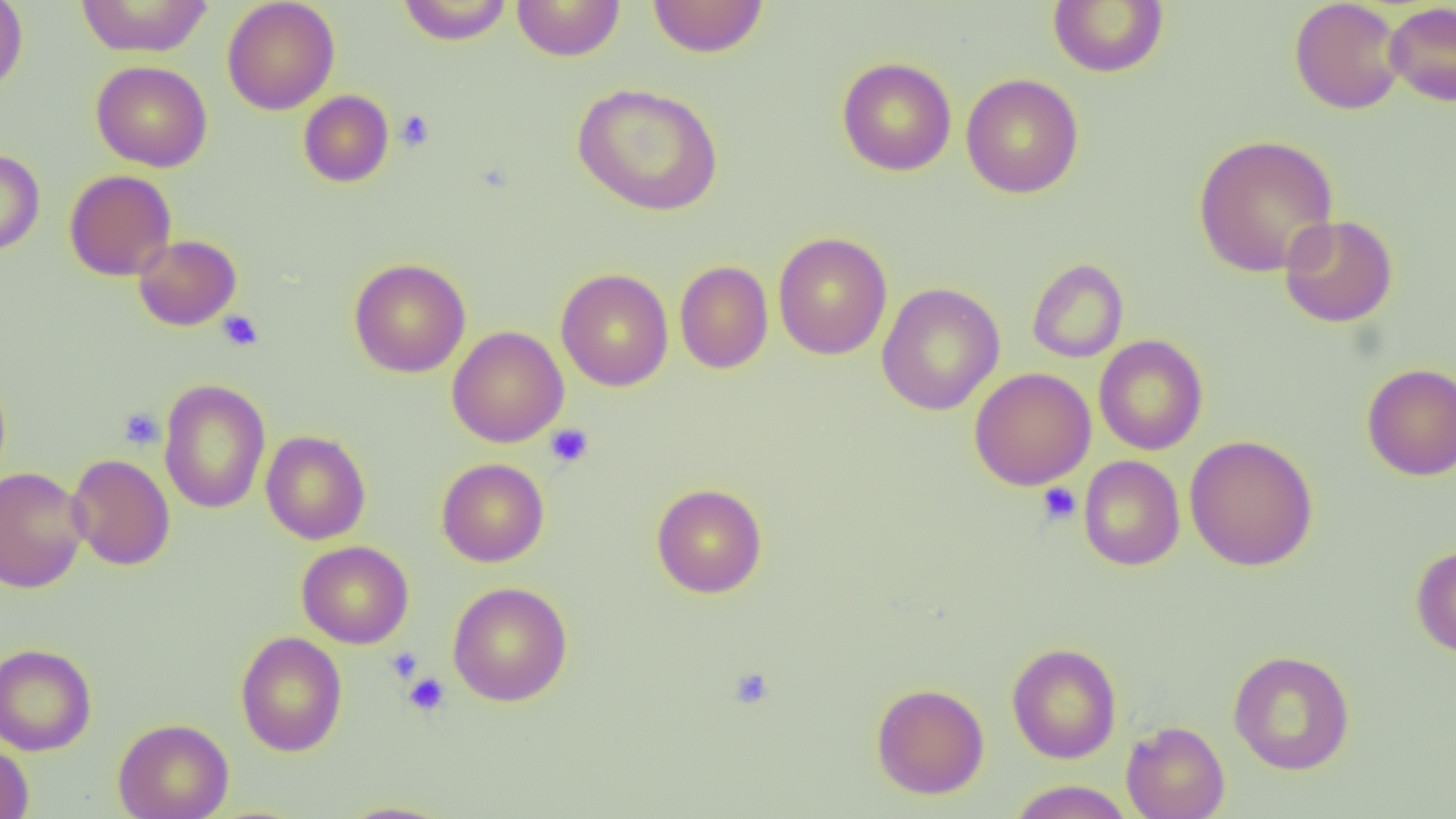
Summary:
  - Coordinate format: approximate bounding boxes as named x1/y1/x2/y2 corners in pixels
  - Platelet locations: (x1=395, y1=110, x2=435, y2=151), (x1=217, y1=310, x2=264, y2=352), (x1=118, y1=408, x2=164, y2=450), (x1=545, y1=423, x2=594, y2=468), (x1=1037, y1=483, x2=1081, y2=526), (x1=386, y1=646, x2=423, y2=683), (x1=728, y1=666, x2=775, y2=710), (x1=403, y1=672, x2=450, y2=716)
  - Uninfected red blood cell locations: (x1=0, y1=0, x2=28, y2=94), (x1=76, y1=0, x2=213, y2=58), (x1=222, y1=0, x2=340, y2=115), (x1=512, y1=0, x2=625, y2=61), (x1=647, y1=0, x2=769, y2=57), (x1=1289, y1=0, x2=1407, y2=115), (x1=397, y1=1, x2=512, y2=45), (x1=1048, y1=1, x2=1169, y2=77), (x1=1384, y1=1, x2=1456, y2=107), (x1=837, y1=57, x2=957, y2=176), (x1=91, y1=60, x2=212, y2=172), (x1=961, y1=73, x2=1084, y2=198), (x1=572, y1=82, x2=723, y2=216), (x1=298, y1=90, x2=394, y2=187), (x1=1193, y1=134, x2=1339, y2=277), (x1=0, y1=148, x2=44, y2=256), (x1=64, y1=169, x2=177, y2=281), (x1=1278, y1=214, x2=1398, y2=328), (x1=773, y1=232, x2=893, y2=360), (x1=132, y1=234, x2=242, y2=331), (x1=673, y1=257, x2=885, y2=369), (x1=348, y1=258, x2=471, y2=378), (x1=1026, y1=258, x2=1129, y2=363), (x1=674, y1=260, x2=774, y2=374), (x1=556, y1=269, x2=673, y2=391), (x1=877, y1=282, x2=1005, y2=415), (x1=447, y1=326, x2=568, y2=447), (x1=1089, y1=335, x2=1191, y2=572), (x1=1094, y1=335, x2=1208, y2=455), (x1=1362, y1=363, x2=1456, y2=480), (x1=969, y1=367, x2=1096, y2=490), (x1=158, y1=378, x2=271, y2=514), (x1=260, y1=430, x2=371, y2=544), (x1=1185, y1=434, x2=1319, y2=571), (x1=67, y1=453, x2=175, y2=570), (x1=1078, y1=455, x2=1185, y2=571), (x1=436, y1=457, x2=549, y2=567), (x1=0, y1=467, x2=89, y2=593), (x1=651, y1=483, x2=767, y2=598), (x1=297, y1=541, x2=413, y2=648), (x1=1411, y1=544, x2=1456, y2=658), (x1=447, y1=581, x2=573, y2=707), (x1=235, y1=631, x2=348, y2=756), (x1=1006, y1=642, x2=1122, y2=763), (x1=0, y1=643, x2=97, y2=756), (x1=1228, y1=649, x2=1356, y2=775), (x1=871, y1=682, x2=989, y2=799), (x1=113, y1=718, x2=234, y2=819), (x1=1121, y1=720, x2=1230, y2=819), (x1=0, y1=742, x2=34, y2=818), (x1=1007, y1=780, x2=1136, y2=818), (x1=335, y1=800, x2=457, y2=818)
  - Slide-level diagnosis: no evidence of blood parasites
  - Modality: optical microscopy
  - Field of view: single
  - Preparation: thin blood smear
  - Image size: 1456×819 pixels
  - Magnification: 1000x